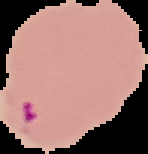

image size = 148×154 pixels
result = Plasmodium parasites detected
preparation = thin blood smear
image type = segmented cell region on a black background